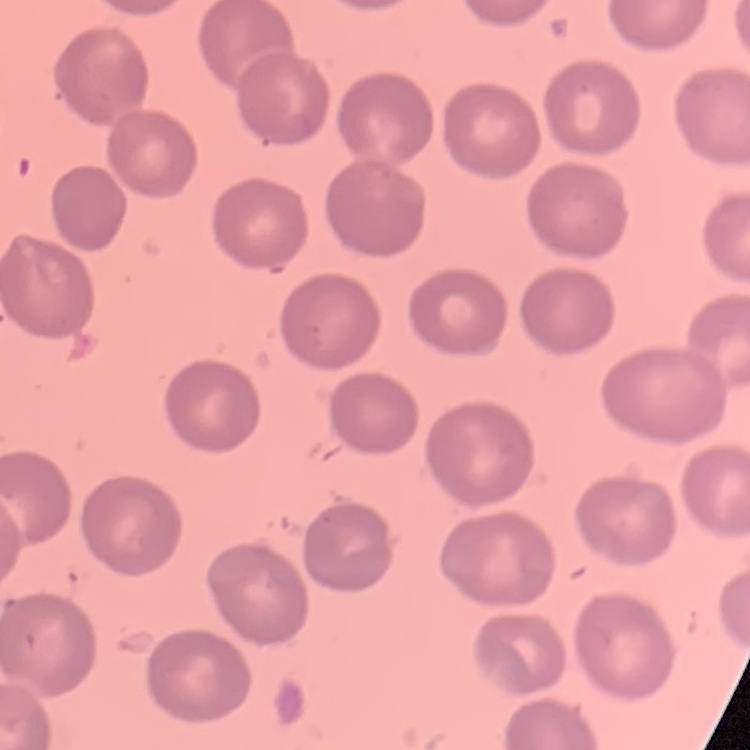

red blood cell morphology = no rouleaux formation
preparation = thin blood film
image type = one tile cut from a larger photomicrograph
stain = Field's or Giemsa